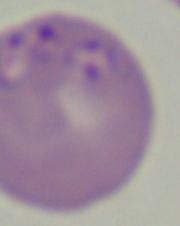

Summary:
  - Magnification: 1000x
  - Identification: Babesia
  - Modality: micrograph